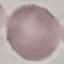 Result: negative for malaria parasites. Giemsa-stained preparation. Automatically extracted cell patch, resized to 64 × 64 pixels. Acquired by smartphone through the microscope eyepiece. Thin blood smear.